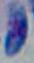 Toxoplasma gondii is seen. Photomicrograph. 1000x magnification.